Outline each blood parasite and name the species.
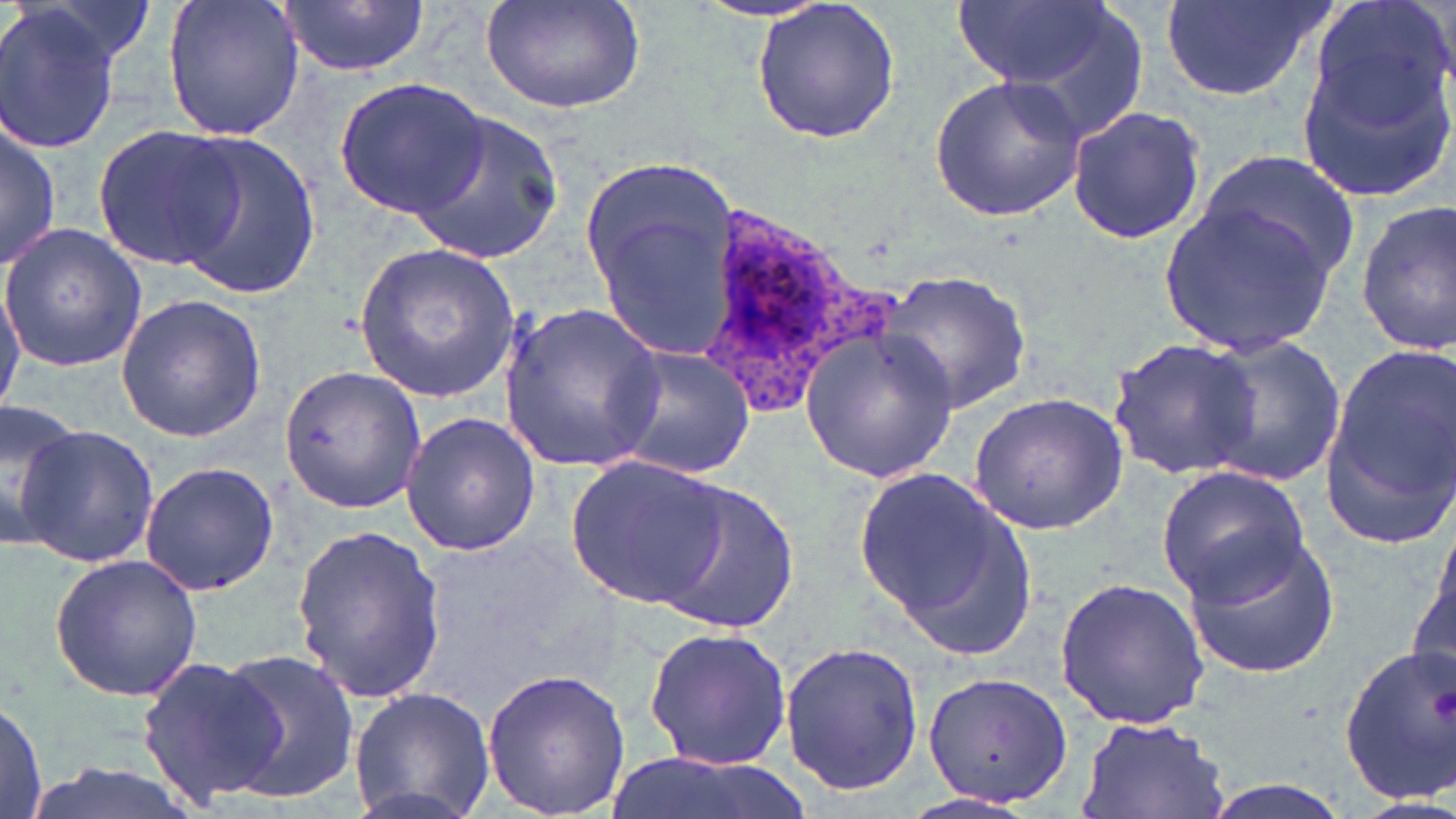

Approximate bounding boxes as [x1, y1, x2, y2] in pixels.
Plasmodium ovale-infected red blood cells: [695, 199, 904, 421].
No Plasmodium falciparum, Plasmodium malariae, Plasmodium vivax, Babesia divergens, or Trypanosoma brucei observed.

slide-level diagnosis = Plasmodium ovale
image size = 1456×819 pixels
preparation = thin blood smear
modality = light microscopy
magnification = 1000x
field of view = one of a larger specimen
stain = May-Grünwald-Giemsa
uninfected red blood cell locations = approximate bounding boxes as [x1, y1, x2, y2] in pixels: [160, 0, 306, 143], [279, 0, 429, 76], [479, 0, 646, 115], [749, 0, 902, 147], [949, 0, 1119, 98], [1162, 0, 1330, 103], [1305, 0, 1456, 141], [0, 3, 124, 153], [1295, 47, 1455, 203], [929, 72, 1086, 222], [335, 79, 489, 217], [1066, 103, 1206, 246], [405, 109, 566, 262], [0, 118, 60, 273], [90, 122, 242, 270], [159, 133, 320, 299], [1195, 146, 1360, 290], [582, 150, 742, 359], [1160, 202, 1338, 358], [1355, 203, 1456, 356], [1, 221, 149, 372], [354, 241, 520, 404], [876, 269, 1031, 412], [0, 271, 27, 410], [115, 293, 267, 442], [497, 298, 665, 473], [801, 325, 956, 485], [1197, 336, 1349, 486], [1107, 338, 1262, 478], [1319, 342, 1456, 537], [607, 344, 755, 479], [278, 364, 424, 512], [965, 393, 1131, 536], [0, 399, 86, 548], [402, 412, 542, 556], [13, 422, 158, 571], [567, 455, 734, 609], [137, 460, 280, 597], [851, 462, 1034, 654], [1156, 465, 1311, 603], [643, 476, 801, 638], [1421, 519, 1456, 665], [291, 523, 446, 702], [1182, 529, 1341, 678], [48, 554, 202, 701], [1054, 576, 1209, 730], [642, 627, 793, 771], [779, 639, 923, 797], [1337, 647, 1456, 803], [210, 649, 361, 804], [135, 654, 284, 810], [480, 667, 630, 818], [921, 669, 1073, 809], [350, 686, 495, 819], [0, 697, 48, 819], [1074, 716, 1233, 819], [600, 749, 798, 819], [21, 757, 204, 819], [1196, 780, 1358, 819]